Classify this cell by malaria status.
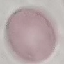
It is uninfected.

Summary:
  - Preparation: thin blood smear
  - Capture: smartphone camera at the microscope eyepiece
  - Image type: automatically extracted cell patch, resized to 64 × 64 pixels
  - Stain: Giemsa